Comment on the morphology of the red blood cells.
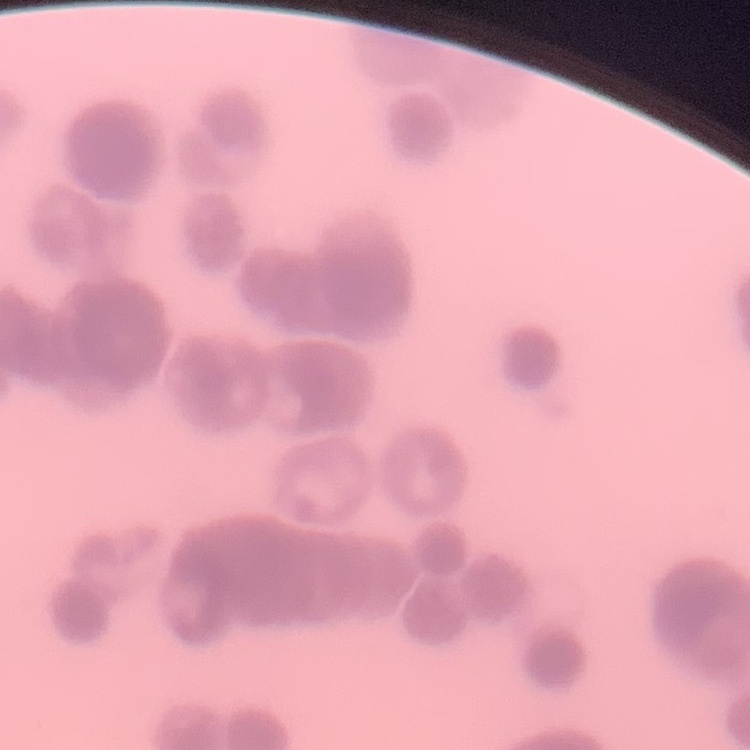

Rouleaux formation.

Summary:
  - Stain: Field's or Giemsa
  - Preparation: thin peripheral smear
  - Image type: one tile cut from a larger photomicrograph